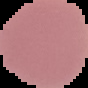
Summary:
  - Preparation: thin blood smear
  - Result: no Plasmodium parasites detected
  - Image size: 88×88 pixels
  - Image type: cell region segmented out of the field of view; surrounding area masked to black